Assess this cell for malaria.
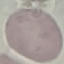

Uninfected.

Summary:
  - Capture: smartphone camera at the microscope eyepiece
  - Image type: automatically extracted cell patch, resized to 64 × 64 pixels
  - Stain: Giemsa
  - Preparation: thin blood film